Locate and identify every blood parasite.
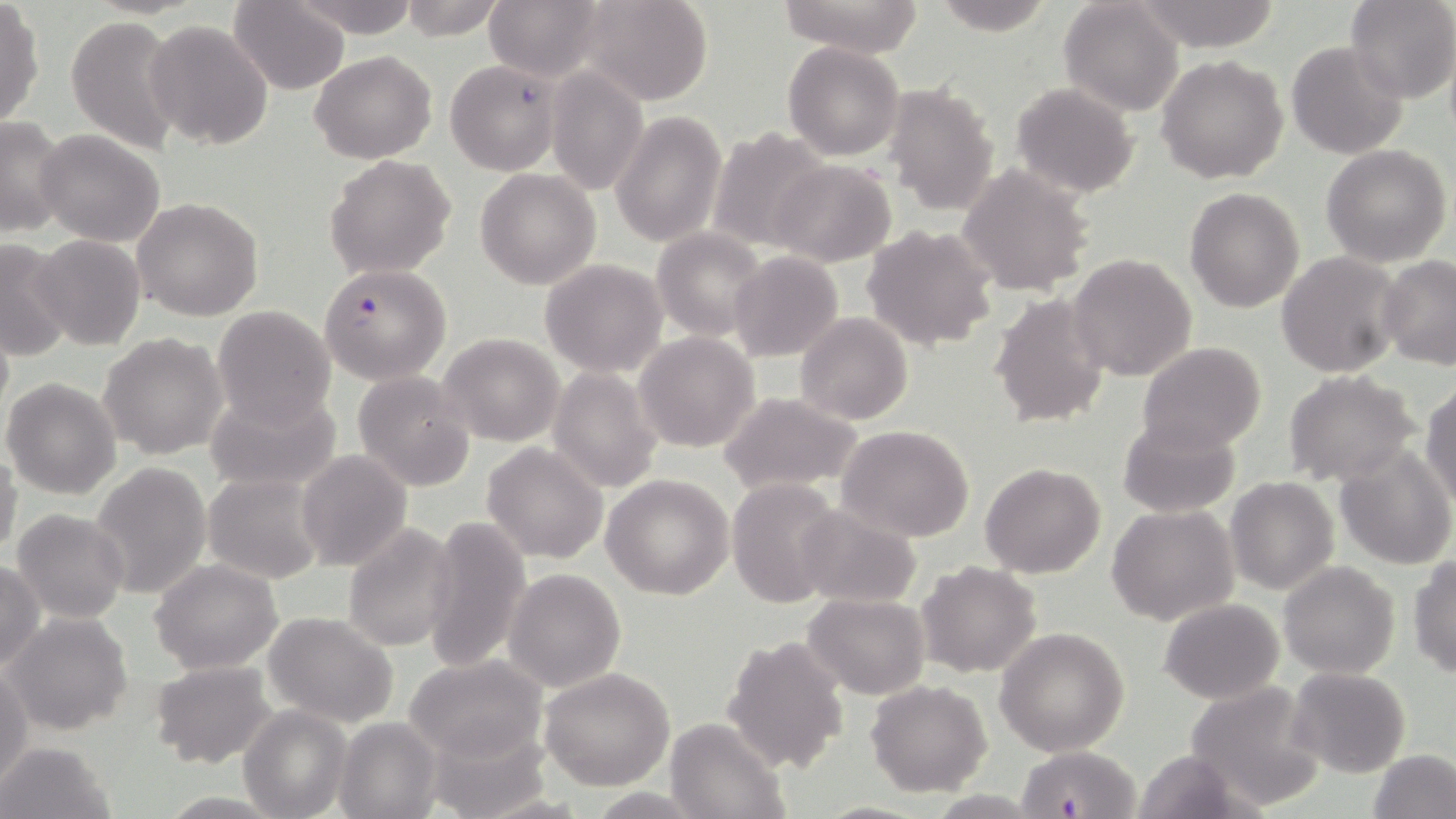

Approximate bounding boxes as (x1, y1, x2, y2) in pixels.
Plasmodium falciparum-infected red blood cells: (319, 265, 451, 384), (1015, 744, 1140, 816).
No Plasmodium ovale, Plasmodium malariae, Plasmodium vivax, Babesia divergens, or Trypanosoma brucei observed.

Uninfected red blood cell locations: (228, 0, 351, 95), (293, 0, 419, 37), (397, 0, 509, 42), (482, 0, 609, 84), (577, 0, 713, 105), (775, 0, 925, 57), (927, 0, 1060, 38), (1135, 0, 1283, 51), (1344, 0, 1455, 103), (1058, 1, 1183, 116), (0, 4, 44, 128), (66, 16, 185, 155), (142, 19, 274, 153), (1286, 41, 1408, 160), (783, 42, 905, 162), (310, 51, 436, 163), (1157, 55, 1288, 183), (446, 59, 562, 176), (545, 65, 648, 197), (1011, 82, 1138, 197), (881, 84, 999, 216), (610, 109, 725, 249), (0, 116, 71, 238), (707, 128, 831, 254), (36, 129, 165, 246), (1322, 144, 1452, 267), (323, 155, 458, 279), (768, 160, 895, 266), (957, 164, 1095, 298), (476, 168, 602, 291), (1184, 188, 1305, 313), (132, 197, 263, 321), (863, 225, 999, 351), (653, 228, 770, 342), (32, 234, 145, 350), (0, 235, 76, 360), (729, 250, 845, 362), (1277, 252, 1403, 376), (1067, 253, 1197, 383), (1379, 255, 1456, 368), (539, 258, 667, 378), (991, 292, 1110, 431), (213, 305, 337, 429), (794, 312, 912, 426), (633, 331, 760, 454), (439, 332, 564, 446), (100, 333, 227, 460), (377, 340, 521, 468), (1138, 342, 1266, 454), (550, 366, 664, 494), (352, 370, 476, 492), (1284, 370, 1420, 487), (2, 378, 121, 499), (1421, 382, 1456, 506), (206, 387, 342, 494), (717, 391, 864, 494), (1117, 417, 1239, 517), (835, 425, 976, 542), (483, 443, 609, 564), (1335, 445, 1455, 570), (0, 447, 23, 561), (296, 449, 412, 570), (91, 461, 212, 600), (980, 463, 1105, 578), (203, 473, 329, 586), (601, 473, 734, 599), (1225, 476, 1340, 594), (728, 478, 846, 610), (794, 503, 925, 609), (1107, 504, 1239, 626), (12, 509, 129, 623), (422, 514, 532, 674), (339, 521, 461, 652), (1409, 556, 1456, 677), (151, 558, 283, 673), (0, 560, 46, 673), (1278, 561, 1400, 679), (917, 562, 1040, 679), (504, 568, 625, 691), (803, 593, 929, 699), (1158, 598, 1284, 704), (264, 611, 401, 728), (6, 612, 132, 736), (995, 627, 1131, 756), (722, 634, 850, 774), (405, 653, 549, 767), (150, 659, 276, 768), (1, 666, 33, 785), (1287, 667, 1412, 777), (539, 669, 677, 789), (866, 680, 992, 796), (1184, 681, 1326, 811), (239, 706, 352, 819), (334, 716, 442, 818), (663, 718, 790, 819), (1, 740, 115, 818), (1370, 749, 1456, 819), (1131, 750, 1253, 818), (156, 792, 287, 818), (810, 800, 934, 818). Slide-level diagnosis: Plasmodium falciparum. Image is 1456×819 pixels. Captured at 1000x magnification. May-Grünwald-Giemsa stain. Light microscopy. Single field of view. Thin blood film.